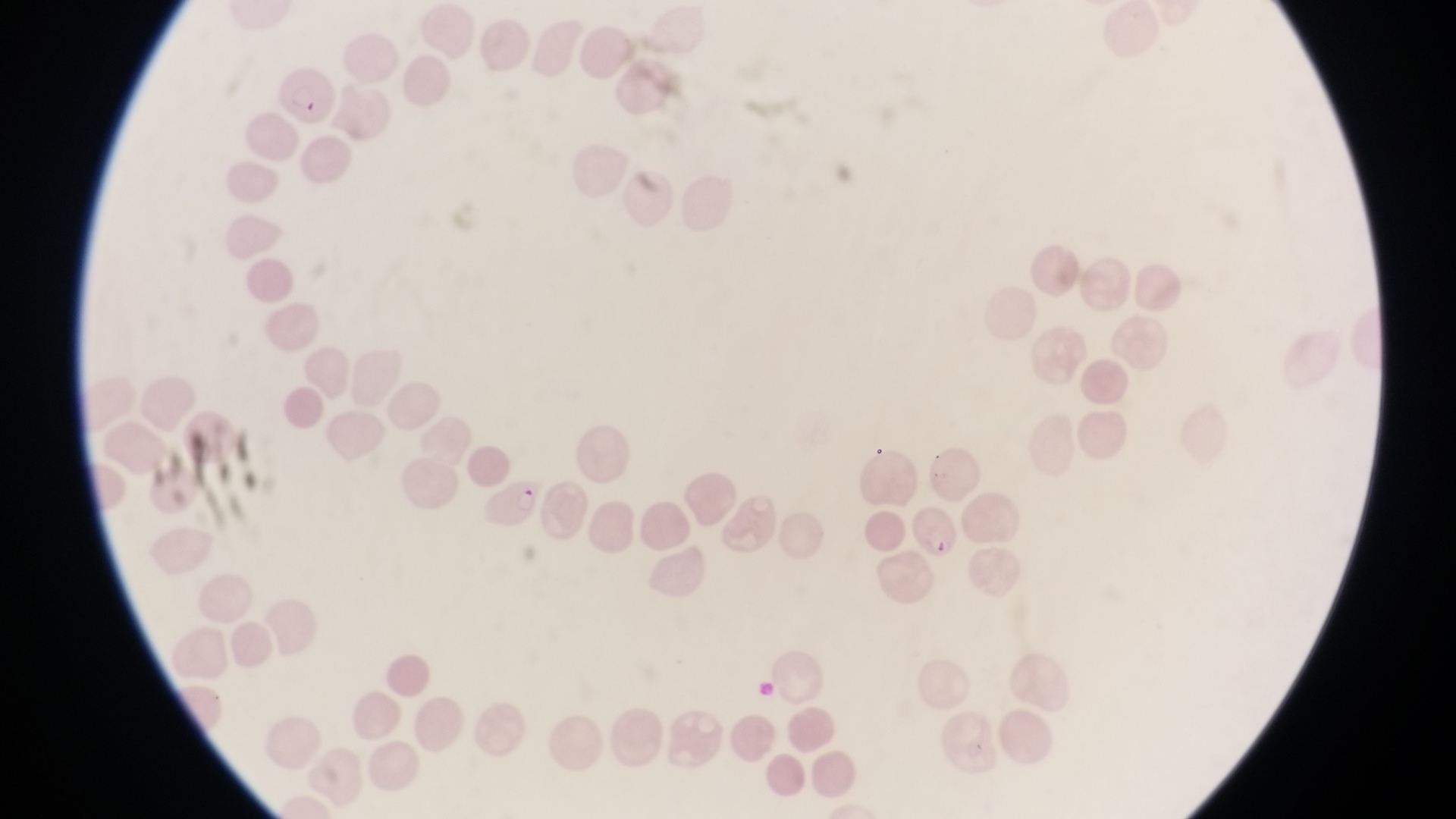 Approximate bounding boxes as {left, top, right, bottom} in pixels. Parasitised red blood cell locations: {275, 69, 338, 129}, {489, 473, 545, 533}, {909, 504, 962, 559}. Thin blood smear. Image is 1456×819 pixels. Sample from Uganda. Captured by a smartphone held over the eyepiece of an Olympus CX-23 microscope. One field of view. Magnification of 1000x.